Locate every blood parasite and identify its species.
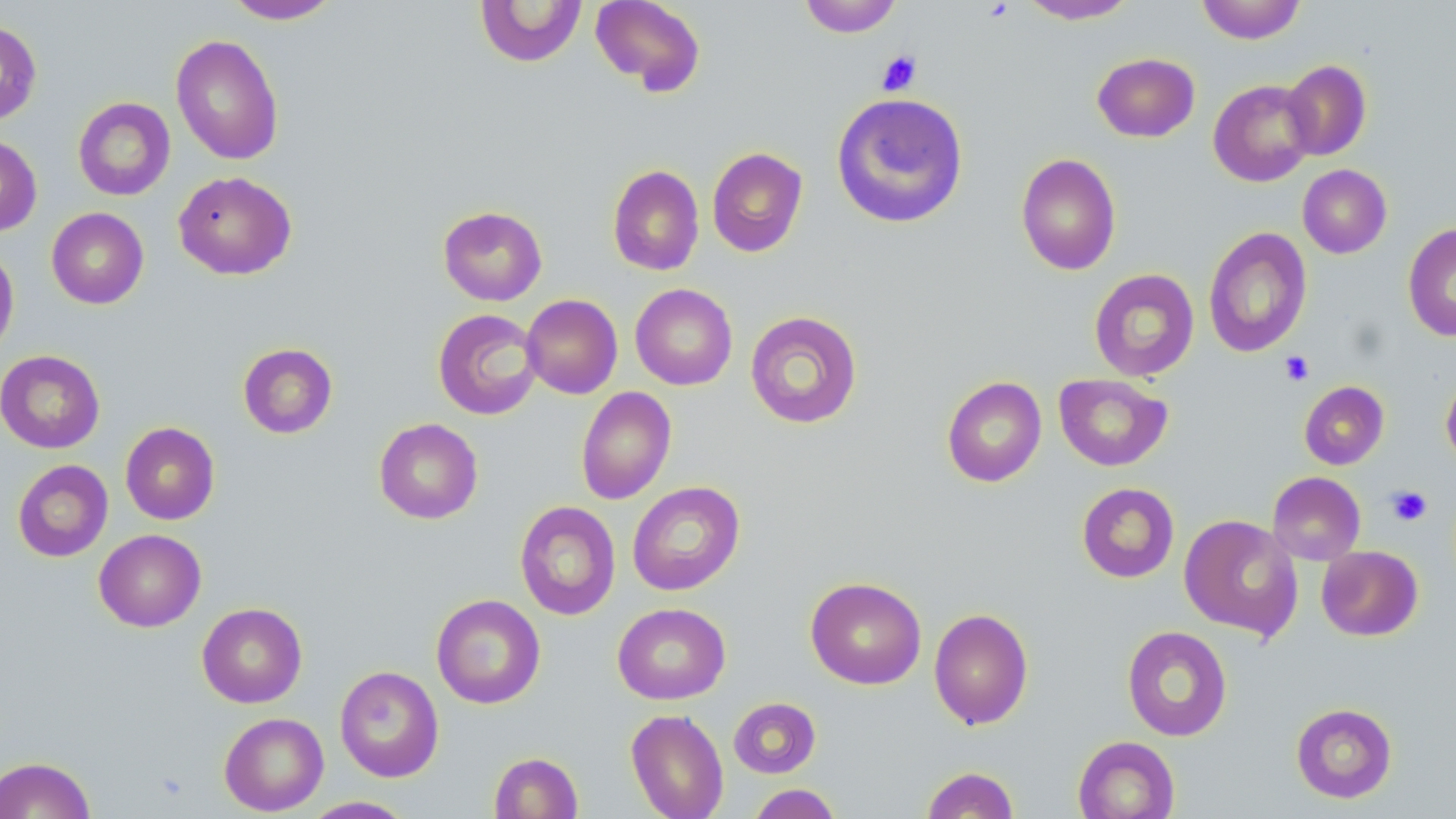

No blood parasites observed.

Approximate bounding boxes as named x1/y1/x2/y2 corners in pixels. Platelet locations: (x1=876, y1=50, x2=922, y2=96), (x1=1280, y1=351, x2=1314, y2=386), (x1=1387, y1=485, x2=1432, y2=526). Uninfected red blood cell locations: (x1=223, y1=0, x2=341, y2=24), (x1=589, y1=0, x2=706, y2=95), (x1=798, y1=0, x2=903, y2=37), (x1=1018, y1=0, x2=1137, y2=24), (x1=1196, y1=0, x2=1307, y2=44), (x1=475, y1=1, x2=587, y2=67), (x1=0, y1=20, x2=42, y2=124), (x1=170, y1=33, x2=285, y2=165), (x1=1092, y1=52, x2=1200, y2=142), (x1=1281, y1=59, x2=1372, y2=161), (x1=1208, y1=79, x2=1317, y2=187), (x1=831, y1=92, x2=969, y2=229), (x1=73, y1=97, x2=175, y2=200), (x1=0, y1=134, x2=42, y2=236), (x1=707, y1=147, x2=808, y2=257), (x1=1015, y1=152, x2=1121, y2=275), (x1=1297, y1=164, x2=1392, y2=258), (x1=607, y1=165, x2=704, y2=276), (x1=173, y1=170, x2=297, y2=280), (x1=437, y1=205, x2=548, y2=306), (x1=46, y1=207, x2=149, y2=309), (x1=1403, y1=223, x2=1456, y2=342), (x1=1203, y1=226, x2=1312, y2=358), (x1=0, y1=243, x2=19, y2=360), (x1=1089, y1=268, x2=1199, y2=381), (x1=630, y1=283, x2=738, y2=390), (x1=521, y1=294, x2=622, y2=399), (x1=433, y1=308, x2=543, y2=420), (x1=745, y1=310, x2=863, y2=428), (x1=238, y1=342, x2=338, y2=438), (x1=0, y1=350, x2=105, y2=453), (x1=1054, y1=373, x2=1172, y2=471), (x1=1441, y1=373, x2=1456, y2=469), (x1=942, y1=376, x2=1047, y2=487), (x1=1299, y1=380, x2=1389, y2=469), (x1=575, y1=386, x2=676, y2=505), (x1=373, y1=418, x2=483, y2=524), (x1=120, y1=422, x2=220, y2=525), (x1=12, y1=459, x2=113, y2=562), (x1=1267, y1=472, x2=1366, y2=565), (x1=627, y1=481, x2=745, y2=596), (x1=1077, y1=482, x2=1179, y2=583), (x1=514, y1=501, x2=621, y2=620), (x1=1179, y1=514, x2=1303, y2=640), (x1=94, y1=529, x2=206, y2=632), (x1=1316, y1=545, x2=1423, y2=641), (x1=805, y1=576, x2=927, y2=689), (x1=431, y1=594, x2=546, y2=709), (x1=196, y1=602, x2=307, y2=708), (x1=612, y1=602, x2=730, y2=704), (x1=928, y1=608, x2=1033, y2=730), (x1=1121, y1=625, x2=1233, y2=741), (x1=334, y1=665, x2=444, y2=782), (x1=728, y1=697, x2=821, y2=778), (x1=1291, y1=702, x2=1398, y2=803), (x1=625, y1=708, x2=729, y2=819), (x1=219, y1=712, x2=328, y2=816), (x1=1073, y1=735, x2=1179, y2=819), (x1=489, y1=752, x2=583, y2=818), (x1=0, y1=756, x2=95, y2=818), (x1=921, y1=766, x2=1019, y2=818), (x1=747, y1=784, x2=843, y2=819), (x1=300, y1=796, x2=417, y2=818). Slide-level diagnosis: no evidence of blood parasites. May-Grünwald-Giemsa stain. Thin blood film. Captured at 1000x magnification. Image is 1456×819 pixels. Optical microscopy. One field of a larger specimen.